Name the blood parasite species.
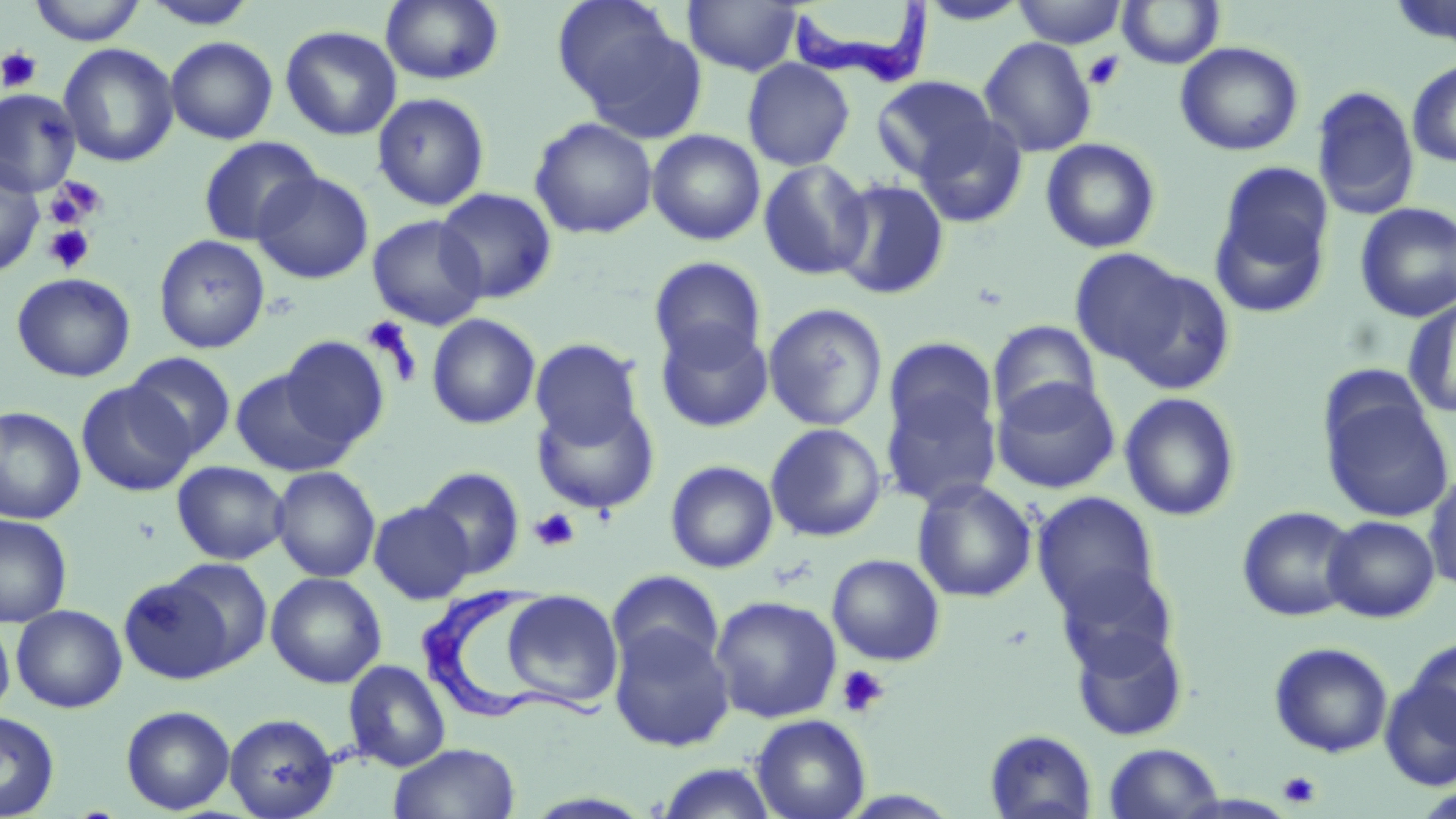

Trypanosoma brucei.

{
  "modality": "light microscopy",
  "trypanosoma_brucei_locations": "approximate bounding boxes as (x1,y1)-(x2,y2) corner pairs in pixels: (784,1)-(935,88), (423,586)-(612,731)",
  "stain": "May-Grünwald-Giemsa",
  "platelet_locations": "approximate bounding boxes as (x1,y1)-(x2,y2) corner pairs in pixels: (0,47)-(42,92), (1083,51)-(1125,91), (45,177)-(105,227), (43,225)-(95,274), (361,315)-(419,379), (529,507)-(580,552), (836,664)-(889,718), (1278,770)-(1322,808)",
  "preparation": "thin blood smear",
  "image_size": "1456×819 pixels",
  "uninfected_red_blood_cell_locations": "approximate bounding boxes as (x1,y1)-(x2,y2) corner pairs in pixels: (29,0)-(146,46), (141,0)-(259,30), (380,0)-(504,85), (551,0)-(684,110), (682,0)-(803,77), (1012,0)-(1126,48), (918,1)-(1031,26), (1117,1)-(1225,69), (576,21)-(710,143), (280,25)-(402,141), (165,36)-(278,144), (979,36)-(1098,158), (1174,41)-(1304,157), (58,42)-(179,168), (742,58)-(855,171), (1406,59)-(1456,168), (871,75)-(998,181), (1311,85)-(1420,220), (0,89)-(81,196), (371,92)-(490,211), (529,116)-(658,239), (914,116)-(1028,229), (646,129)-(766,246), (197,135)-(323,247), (1040,137)-(1162,253), (757,159)-(874,281), (0,160)-(45,277), (1209,166)-(1334,319), (253,171)-(373,284), (833,178)-(950,301), (435,188)-(557,303), (1354,202)-(1456,322), (367,214)-(488,329), (153,234)-(270,354), (1068,248)-(1193,370), (649,256)-(767,367), (1108,264)-(1236,396), (11,272)-(136,382), (1402,298)-(1456,418), (763,303)-(888,432), (426,313)-(541,430), (655,320)-(774,433), (987,320)-(1102,427), (279,336)-(390,450), (883,337)-(999,450), (530,338)-(644,447), (125,353)-(236,458), (230,367)-(355,477), (880,376)-(1002,509), (991,376)-(1120,494), (76,380)-(196,496), (1119,391)-(1242,522), (1323,392)-(1454,523), (531,399)-(659,515), (0,406)-(86,525), (764,423)-(887,542), (665,459)-(778,573), (172,461)-(289,565), (270,466)-(380,582), (418,467)-(525,579), (1424,468)-(1456,594), (911,478)-(1038,603), (1032,492)-(1162,623), (369,501)-(475,604), (1237,505)-(1360,622), (0,514)-(73,627), (1322,515)-(1440,623), (827,553)-(946,666), (161,557)-(274,670), (1052,563)-(1182,677), (607,570)-(725,675), (266,572)-(386,688), (118,574)-(236,685), (500,589)-(623,709), (710,595)-(842,723), (11,604)-(127,713), (0,619)-(15,720), (1069,623)-(1190,742), (609,624)-(735,752), (1405,636)-(1456,750), (1269,641)-(1393,758), (343,659)-(451,772), (1380,678)-(1455,791), (120,705)-(235,814), (0,711)-(60,818), (224,713)-(338,818), (751,714)-(871,819), (984,729)-(1098,819), (388,742)-(521,819), (1103,742)-(1225,819), (653,762)-(781,819)",
  "field_of_view": "one of a larger specimen",
  "magnification": "1000x"
}